Give the extent of all Plasmodium vivax-infected red blood cells.
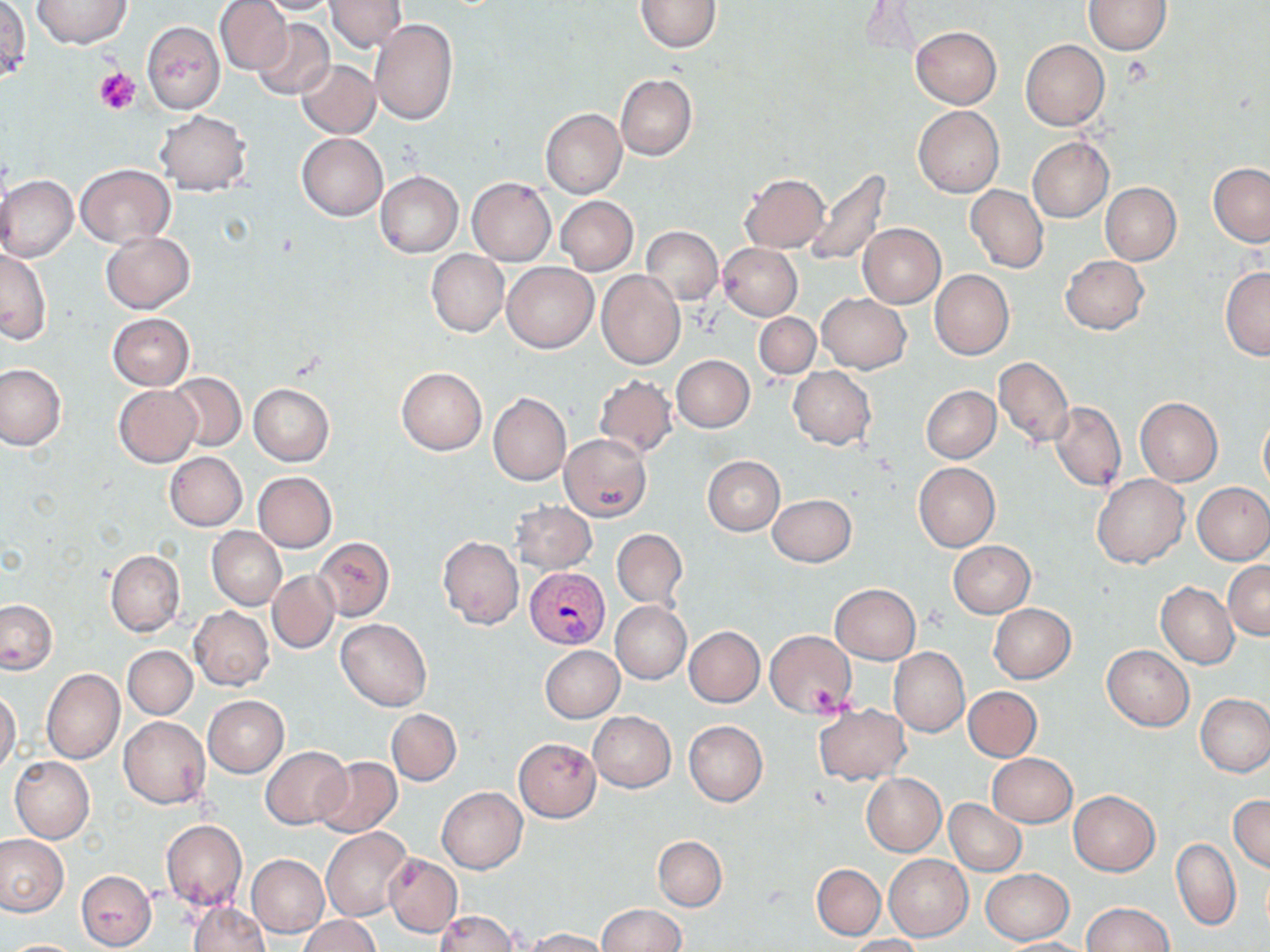

Approximate bounding boxes as named x1/y1/x2/y2 corners in pixels.
Plasmodium vivax-infected red blood cells: (x1=524, y1=566, x2=608, y2=649).

Summary:
  - Platelet locations: (x1=95, y1=68, x2=140, y2=114), (x1=809, y1=679, x2=855, y2=717)
  - Uninfected red blood cell locations: (x1=215, y1=0, x2=292, y2=75), (x1=253, y1=0, x2=342, y2=15), (x1=324, y1=0, x2=406, y2=53), (x1=635, y1=0, x2=721, y2=52), (x1=31, y1=1, x2=130, y2=49), (x1=1084, y1=1, x2=1172, y2=55), (x1=2, y1=4, x2=31, y2=82), (x1=251, y1=18, x2=334, y2=101), (x1=370, y1=18, x2=458, y2=125), (x1=143, y1=21, x2=224, y2=114), (x1=910, y1=26, x2=1001, y2=110), (x1=1020, y1=39, x2=1111, y2=130), (x1=296, y1=58, x2=380, y2=138), (x1=615, y1=73, x2=697, y2=161), (x1=913, y1=106, x2=1003, y2=198), (x1=540, y1=108, x2=626, y2=198), (x1=156, y1=110, x2=250, y2=196), (x1=297, y1=133, x2=388, y2=220), (x1=1027, y1=137, x2=1113, y2=222), (x1=1208, y1=162, x2=1270, y2=246), (x1=76, y1=164, x2=174, y2=247), (x1=802, y1=167, x2=893, y2=267), (x1=375, y1=171, x2=463, y2=257), (x1=739, y1=172, x2=828, y2=253), (x1=0, y1=175, x2=78, y2=262), (x1=468, y1=178, x2=555, y2=265), (x1=1100, y1=182, x2=1181, y2=266), (x1=965, y1=184, x2=1048, y2=273), (x1=556, y1=196, x2=637, y2=275), (x1=857, y1=223, x2=945, y2=308), (x1=641, y1=226, x2=724, y2=305), (x1=101, y1=231, x2=194, y2=313), (x1=718, y1=244, x2=802, y2=320), (x1=1, y1=249, x2=51, y2=343), (x1=426, y1=250, x2=509, y2=336), (x1=1061, y1=255, x2=1149, y2=335), (x1=502, y1=262, x2=597, y2=353), (x1=1220, y1=267, x2=1270, y2=360), (x1=930, y1=269, x2=1014, y2=359), (x1=596, y1=271, x2=685, y2=370), (x1=816, y1=293, x2=909, y2=373), (x1=754, y1=312, x2=820, y2=379), (x1=106, y1=313, x2=193, y2=391), (x1=671, y1=355, x2=755, y2=433), (x1=994, y1=356, x2=1073, y2=448), (x1=0, y1=364, x2=68, y2=451), (x1=396, y1=367, x2=487, y2=454), (x1=788, y1=367, x2=876, y2=449), (x1=165, y1=372, x2=247, y2=451), (x1=594, y1=374, x2=678, y2=460), (x1=248, y1=383, x2=334, y2=466), (x1=114, y1=385, x2=200, y2=467), (x1=922, y1=385, x2=1000, y2=463), (x1=488, y1=393, x2=571, y2=485), (x1=1135, y1=397, x2=1223, y2=485), (x1=1049, y1=402, x2=1126, y2=491), (x1=1258, y1=415, x2=1270, y2=494), (x1=561, y1=434, x2=652, y2=522), (x1=165, y1=451, x2=248, y2=531), (x1=703, y1=456, x2=784, y2=536), (x1=914, y1=462, x2=1000, y2=551), (x1=253, y1=472, x2=337, y2=551), (x1=1093, y1=473, x2=1189, y2=568), (x1=1193, y1=482, x2=1270, y2=565), (x1=768, y1=495, x2=857, y2=567), (x1=511, y1=500, x2=596, y2=573), (x1=207, y1=527, x2=286, y2=610), (x1=612, y1=529, x2=687, y2=609), (x1=437, y1=536, x2=524, y2=629), (x1=314, y1=537, x2=394, y2=621), (x1=947, y1=540, x2=1036, y2=617), (x1=106, y1=549, x2=185, y2=637), (x1=1224, y1=561, x2=1269, y2=640), (x1=267, y1=570, x2=338, y2=654), (x1=1156, y1=582, x2=1239, y2=669), (x1=831, y1=584, x2=921, y2=664), (x1=0, y1=599, x2=57, y2=673), (x1=610, y1=601, x2=691, y2=684), (x1=988, y1=603, x2=1076, y2=683), (x1=189, y1=607, x2=274, y2=691), (x1=336, y1=618, x2=431, y2=710), (x1=685, y1=626, x2=765, y2=707), (x1=765, y1=629, x2=857, y2=719), (x1=1102, y1=645, x2=1194, y2=731), (x1=123, y1=646, x2=197, y2=719), (x1=541, y1=646, x2=624, y2=723), (x1=889, y1=648, x2=969, y2=737), (x1=42, y1=669, x2=125, y2=765), (x1=964, y1=686, x2=1042, y2=762), (x1=0, y1=690, x2=20, y2=775), (x1=1195, y1=693, x2=1270, y2=777), (x1=203, y1=695, x2=289, y2=777), (x1=814, y1=702, x2=909, y2=785), (x1=388, y1=709, x2=462, y2=785), (x1=588, y1=711, x2=675, y2=792), (x1=119, y1=716, x2=210, y2=809), (x1=684, y1=721, x2=768, y2=807), (x1=513, y1=737, x2=601, y2=822), (x1=260, y1=746, x2=351, y2=831), (x1=988, y1=753, x2=1077, y2=827), (x1=9, y1=756, x2=94, y2=843), (x1=313, y1=756, x2=402, y2=838), (x1=862, y1=773, x2=946, y2=856), (x1=436, y1=787, x2=526, y2=873), (x1=1069, y1=790, x2=1160, y2=876), (x1=1229, y1=794, x2=1270, y2=873), (x1=945, y1=799, x2=1026, y2=875), (x1=160, y1=819, x2=247, y2=912), (x1=321, y1=827, x2=411, y2=921), (x1=0, y1=834, x2=68, y2=916), (x1=653, y1=836, x2=727, y2=911), (x1=1171, y1=837, x2=1241, y2=931), (x1=384, y1=853, x2=462, y2=936), (x1=883, y1=853, x2=973, y2=940), (x1=247, y1=854, x2=330, y2=936), (x1=812, y1=863, x2=885, y2=939), (x1=75, y1=869, x2=157, y2=951), (x1=980, y1=869, x2=1075, y2=945), (x1=186, y1=900, x2=269, y2=951), (x1=1081, y1=902, x2=1175, y2=952), (x1=597, y1=904, x2=686, y2=951), (x1=433, y1=909, x2=518, y2=952), (x1=299, y1=915, x2=382, y2=952), (x1=521, y1=927, x2=613, y2=952), (x1=843, y1=934, x2=923, y2=952), (x1=997, y1=937, x2=1092, y2=950), (x1=4, y1=938, x2=85, y2=951)
  - Slide-level diagnosis: Plasmodium vivax
  - Stain: May-Grünwald-Giemsa
  - Magnification: 1000x
  - Image size: 1270×952 pixels
  - Preparation: thin blood smear
  - Modality: optical microscopy
  - Field of view: one of a larger specimen